Assess this cell for malaria.
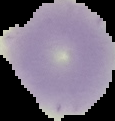

It is uninfected.

Image is 115×121 pixels. Segmented cell region on a black background. From a thin blood smear.